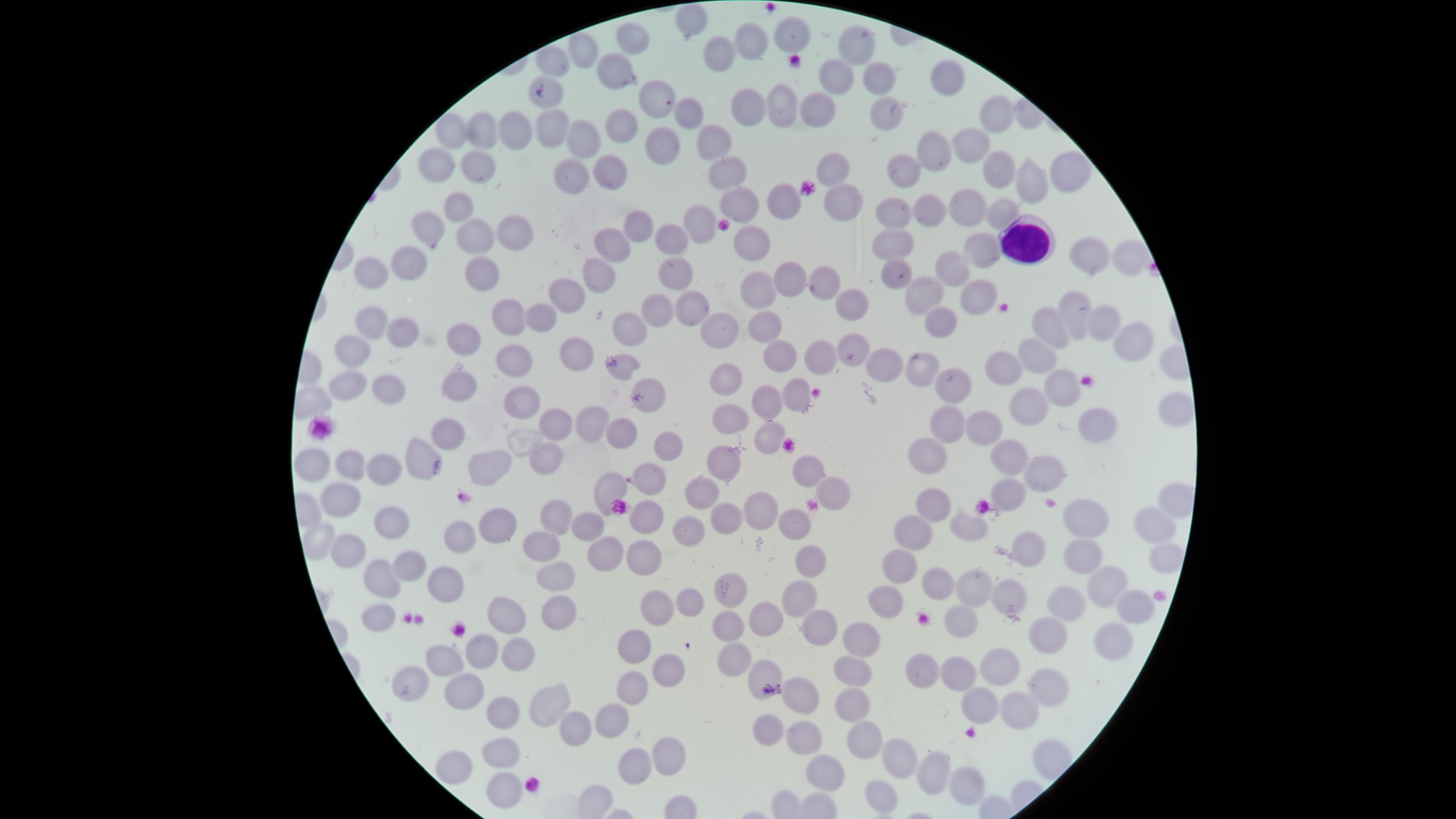

Approximate marker points as (x, y) in pixels. WBCs: (1024, 242). Uninfected RBCs: (692, 19), (793, 33), (629, 37), (747, 37), (854, 41), (586, 50), (722, 51), (556, 65), (613, 68), (880, 74), (831, 75), (944, 77), (547, 90), (655, 95), (782, 102), (747, 106), (810, 107), (685, 113), (890, 115), (994, 115), (452, 124), (548, 125), (618, 126), (509, 127), (478, 129), (576, 135), (706, 141), (968, 142), (663, 143), (931, 147), (434, 163), (479, 166), (830, 168), (900, 168), (997, 168), (1069, 168), (563, 172), (605, 173), (722, 177), (1026, 180), (789, 195), (839, 198), (458, 201), (735, 202), (966, 208), (1000, 208), (929, 211), (896, 212), (701, 219), (433, 226), (634, 231), (511, 233), (670, 240), (755, 240), (477, 241), (893, 241), (606, 243), (979, 243), (1088, 253), (407, 257), (1124, 258), (952, 266), (374, 269), (482, 271), (677, 271), (893, 271), (592, 272), (786, 274), (756, 280), (822, 282), (965, 292), (572, 294), (924, 294), (1079, 305), (661, 306), (686, 306), (545, 310), (842, 310), (504, 314), (370, 318), (938, 318), (1099, 322), (623, 325), (717, 326), (1055, 327), (766, 328), (399, 333), (460, 335), (1124, 341), (857, 348), (352, 349), (574, 352), (782, 353), (1036, 354), (823, 355), (509, 357), (887, 362), (925, 362), (621, 363), (1007, 365), (949, 375), (1062, 377), (725, 379), (456, 381), (348, 382), (385, 390), (796, 394), (650, 395), (762, 395), (519, 401), (1027, 407), (1177, 410), (729, 418), (946, 418), (1099, 419), (590, 421), (551, 425), (986, 425), (624, 430), (448, 432), (768, 433), (669, 442), (418, 448), (928, 449), (1007, 452), (316, 456), (489, 459), (539, 459), (724, 460), (345, 462), (1043, 466), (379, 467), (806, 467), (655, 472), (612, 483), (1010, 488), (707, 489), (836, 489), (345, 495), (928, 502), (757, 509), (728, 516), (561, 517), (790, 518), (1091, 519), (392, 520), (646, 520), (497, 525), (686, 525), (969, 525), (585, 526), (1147, 526), (457, 535), (911, 535), (318, 537), (540, 543), (345, 550), (1029, 550), (604, 552), (642, 552), (1082, 557), (1156, 559), (408, 563), (809, 563), (900, 563), (444, 571), (378, 574), (553, 574), (939, 580), (1101, 586), (971, 588), (729, 589), (1005, 594), (800, 597), (689, 599), (888, 602), (1071, 605), (1122, 605), (653, 607), (555, 610), (509, 614), (961, 617), (372, 618), (767, 620), (726, 624), (813, 626), (1048, 639), (1104, 641), (862, 642), (632, 647), (480, 650), (510, 650), (733, 655), (441, 663), (999, 663), (763, 670), (853, 670), (930, 671), (667, 672), (952, 672), (405, 681), (632, 682), (1046, 684), (464, 685), (807, 697), (538, 703), (850, 707), (979, 707), (497, 709), (1022, 711), (607, 715), (769, 723), (579, 724), (800, 741), (855, 742), (498, 748), (665, 751), (893, 756), (627, 762), (929, 766), (453, 768), (821, 773), (963, 777), (504, 791), (870, 797). Photographed with a smartphone camera through the microscope eyepiece. Thin blood film. Giemsa stain. Image is 1456×819 pixels. Single field of view. Presence: no malaria parasites detected. The visible region is circular.